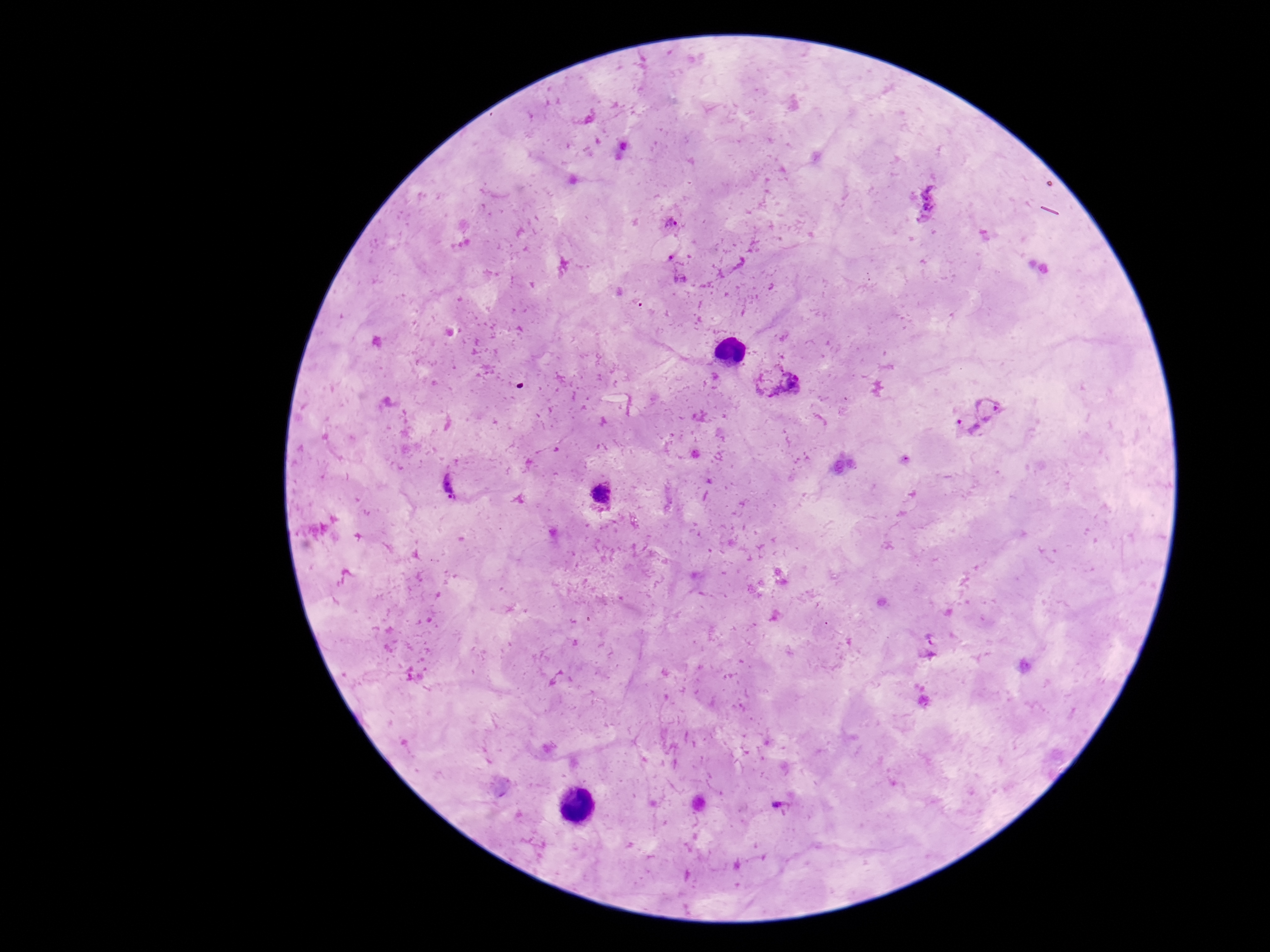

plasmodium_parasite_locations: 'approximate centers as {x, y} in pixels: {930, 200}, {672, 224}, {678, 265}, {791, 382}, {977, 414}, {448, 484}, {602, 495}, {932, 646}, {781, 807}'
capture: smartphone camera through the microscope eyepiece
stain: Giemsa
image_size: 1270×952 pixels
magnification: 100x
preparation: thick blood smear
patient_malaria_status: infected
field_of_view: one from this slide